Assess this cell for malaria.
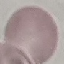

It is uninfected.

{
  "image_type": "cell patch, automatically extracted from a larger field of view and resized to 64 × 64 pixels",
  "capture": "smartphone through the microscope eyepiece",
  "stain": "Giemsa",
  "preparation": "thin blood smear"
}